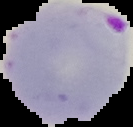

{
  "result": "malaria parasites identified",
  "preparation": "thin blood film",
  "image_type": "cell region segmented out of the field of view; surrounding area masked to black",
  "image_size": "133×127 pixels"
}